Report the malaria status.
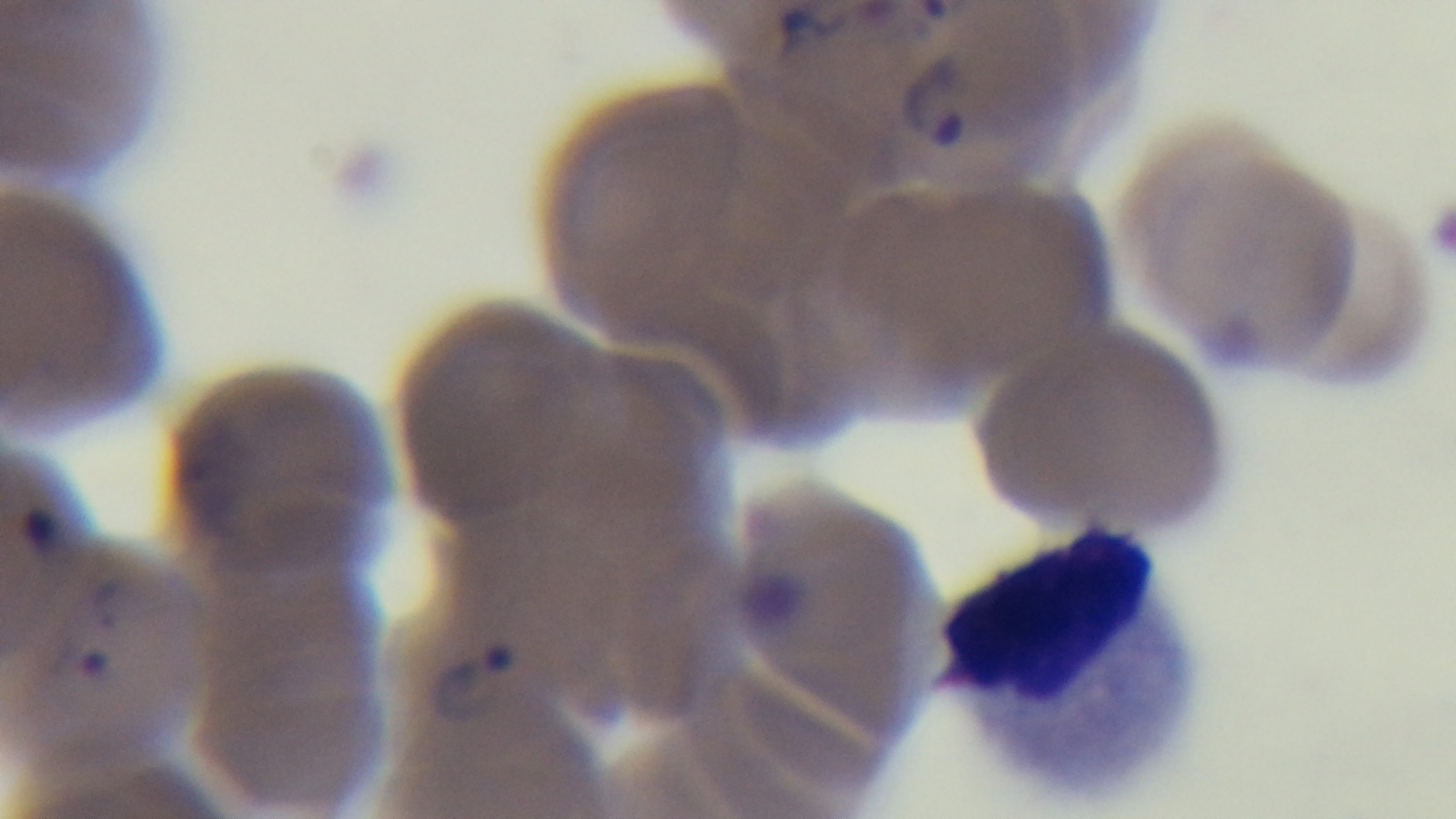

Positive.

Summary:
  - Preparation: thin blood film
  - Modality: light microscopy
  - Stain: Giemsa
  - Capture: mounted 4K digital camera
  - Field of view: single
  - Objective: 100x oil immersion